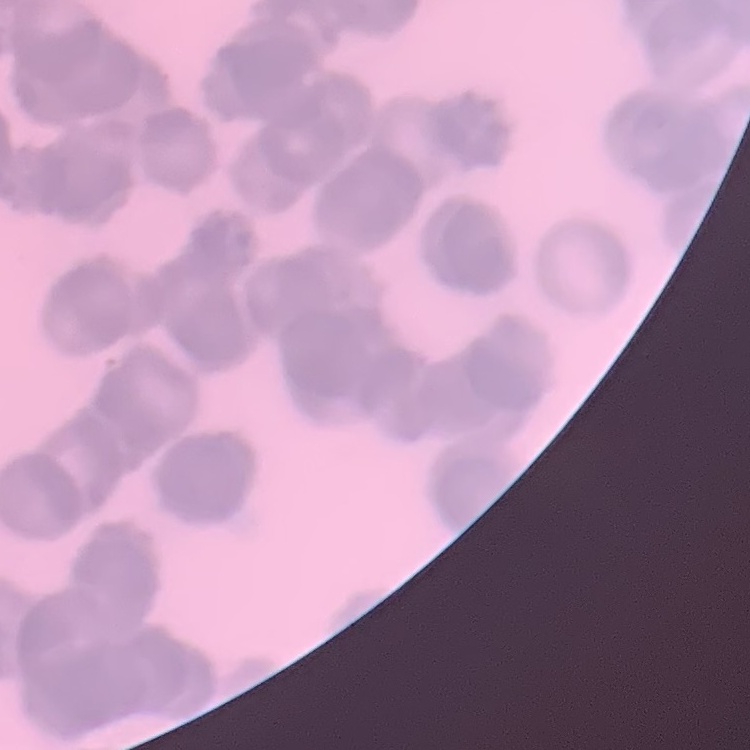

The erythrocytes show rouleaux formation. Thin blood film. Field's or Giemsa stain. Square crop of a larger photomicrograph.